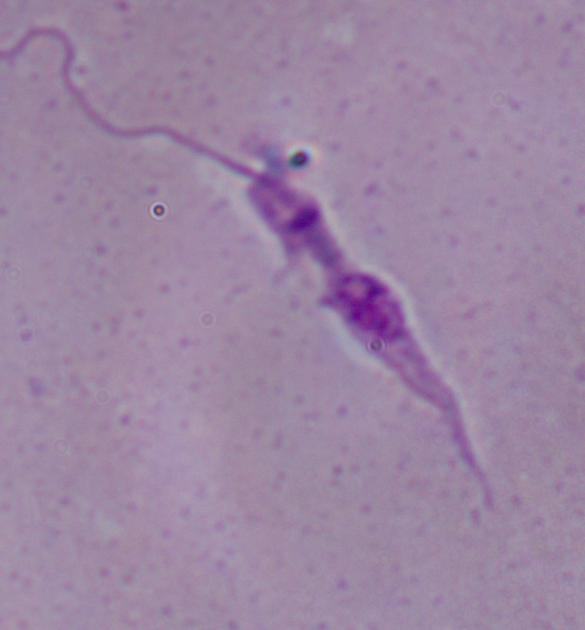

{
  "modality": "micrograph",
  "magnification": "1000x",
  "identification": "Leishmania"
}